Name the blood parasite species.
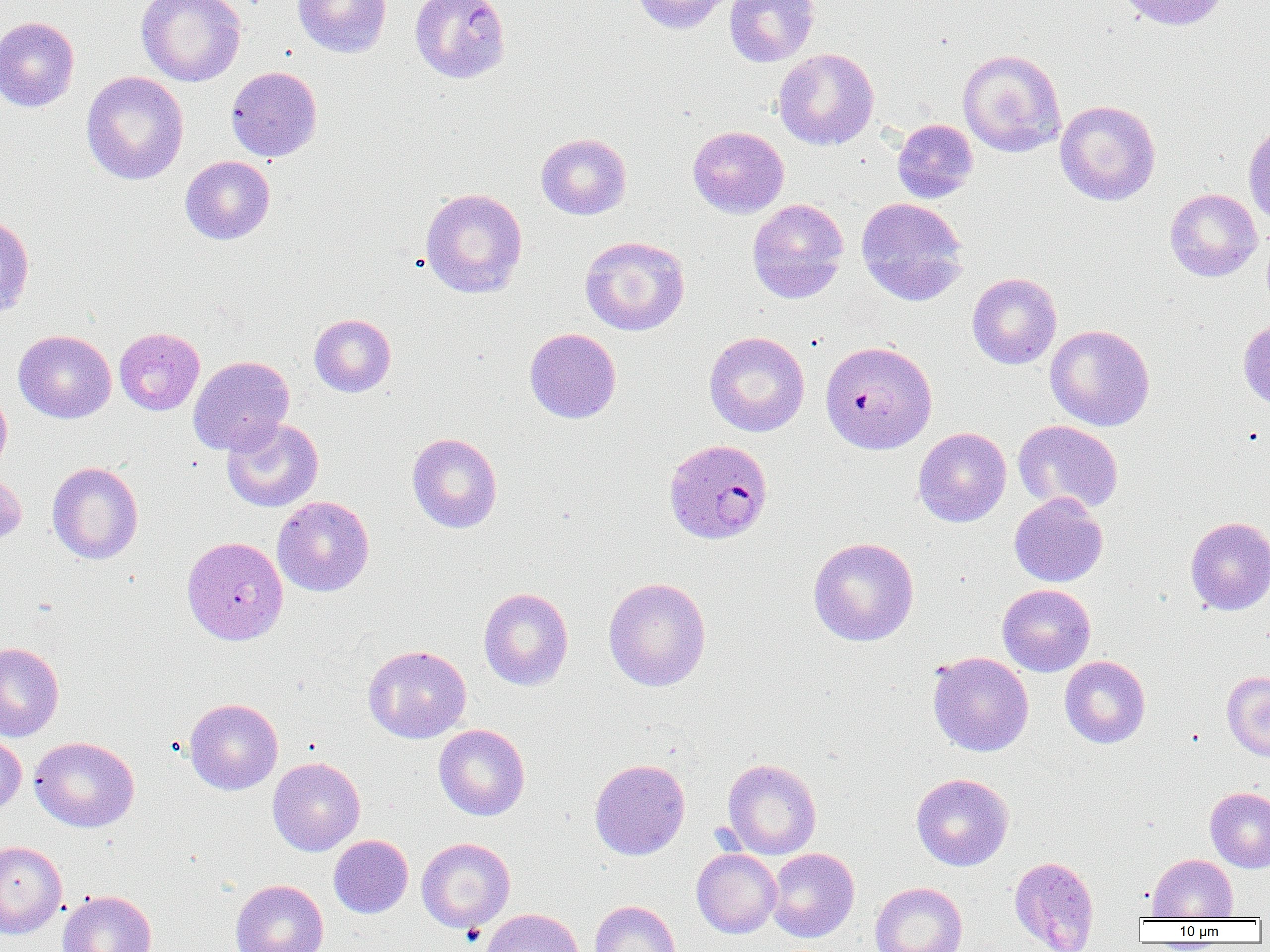
Plasmodium falciparum.

Summary:
  - Coordinate format: approximate bounding boxes as (x1, y1, x2, y2) in pixels
  - Plasmodium falciparum-infected red blood cell locations: (819, 340, 937, 454), (663, 439, 773, 545)
  - Uninfected red blood cell locations: (137, 0, 245, 87), (293, 0, 392, 58), (409, 0, 511, 84), (631, 0, 733, 35), (724, 0, 820, 66), (1116, 0, 1230, 31), (0, 16, 79, 112), (773, 48, 879, 150), (957, 49, 1066, 157), (226, 66, 322, 162), (81, 71, 188, 185), (1055, 100, 1160, 205), (892, 119, 978, 203), (1242, 120, 1270, 227), (688, 125, 789, 218), (536, 133, 631, 220), (180, 155, 275, 245), (420, 188, 527, 298), (1165, 188, 1262, 282), (856, 197, 969, 306), (747, 199, 849, 303), (0, 213, 34, 320), (580, 236, 690, 336), (967, 272, 1062, 369), (309, 314, 396, 397), (1238, 317, 1270, 413), (1045, 324, 1155, 431), (114, 327, 204, 416), (525, 327, 621, 424), (13, 329, 116, 423), (704, 331, 810, 437), (187, 356, 294, 455), (0, 386, 12, 477), (221, 417, 323, 512), (1013, 420, 1124, 514), (913, 427, 1011, 527), (407, 432, 502, 533), (47, 461, 143, 564), (0, 469, 27, 550), (1009, 492, 1108, 587), (272, 495, 374, 597), (1185, 516, 1270, 615), (181, 536, 288, 645), (808, 537, 920, 646), (603, 577, 712, 691), (997, 583, 1095, 676), (478, 587, 573, 690), (0, 642, 64, 742), (362, 645, 472, 744), (928, 652, 1034, 757), (1059, 656, 1151, 748), (1221, 671, 1270, 760), (184, 698, 283, 794), (433, 724, 530, 821), (0, 732, 26, 815), (29, 736, 140, 832), (267, 756, 365, 856), (589, 758, 690, 860), (722, 758, 821, 859), (912, 773, 1014, 871), (1205, 787, 1270, 873), (328, 835, 413, 918), (416, 837, 515, 933), (0, 841, 67, 938), (766, 847, 860, 942), (692, 848, 781, 938), (1148, 853, 1238, 921), (1009, 856, 1099, 952), (231, 879, 328, 952), (870, 881, 967, 952), (58, 890, 157, 952), (590, 900, 680, 952), (480, 908, 584, 952)
  - Field of view: single
  - Modality: optical microscopy
  - Preparation: thin blood film
  - Image size: 1270×952 pixels
  - Magnification: 1000x